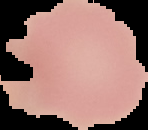
{
  "image_size": "148×130 pixels",
  "malaria_status": "uninfected",
  "image_type": "segmented cell region with the area outside set to black",
  "preparation": "thin blood film"
}